Identify the cell.
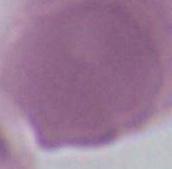

This is an erythrocyte.

Summary:
  - Modality: photomicrograph
  - Magnification: 1000x